Give the extent of all Plasmodium falciparum-infected red blood cells.
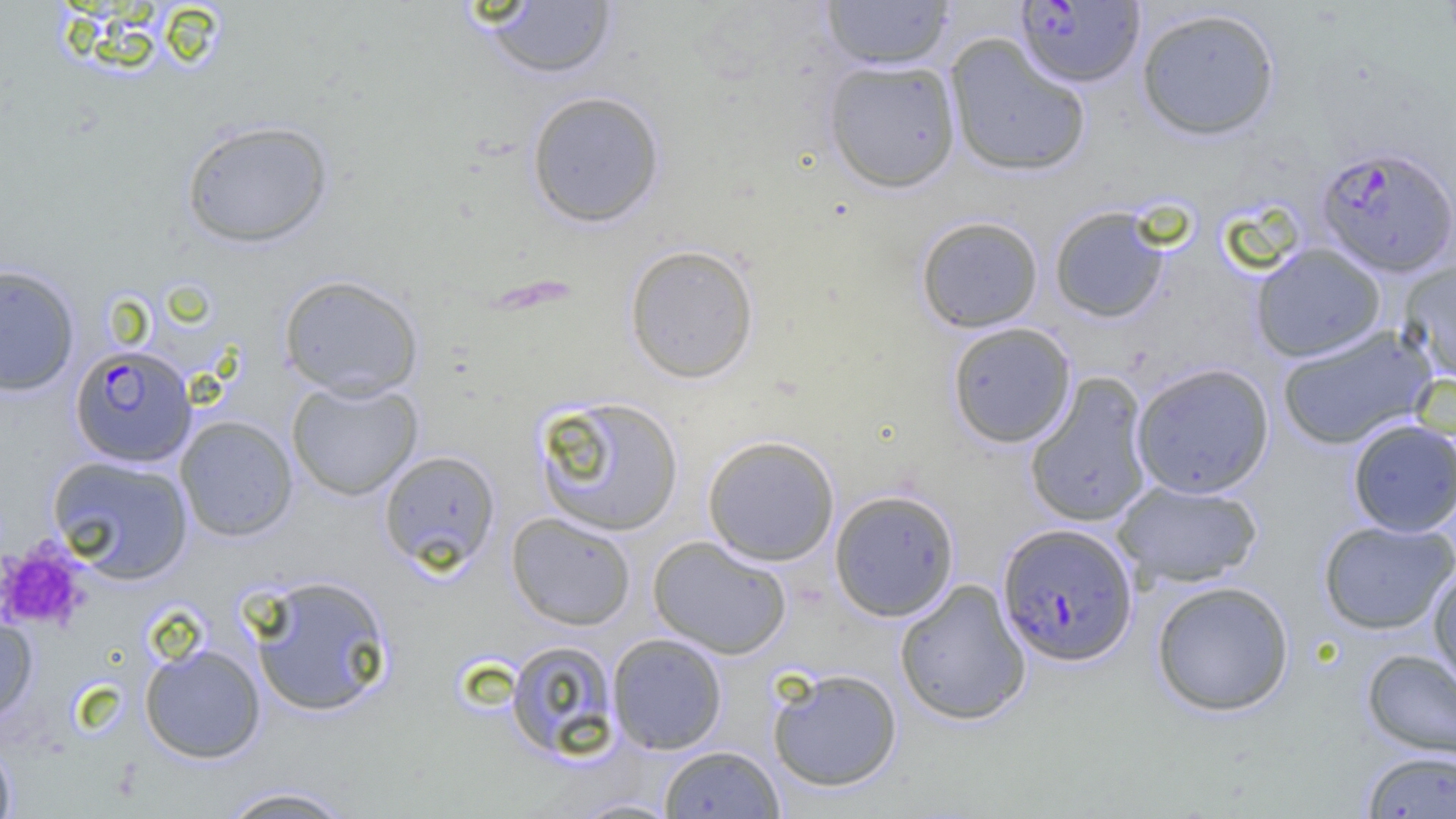

Approximate bounding boxes as [x1, y1, x2, y2] in pixels.
Plasmodium falciparum-infected red blood cells: [1016, 1, 1145, 88], [1316, 145, 1455, 278], [70, 344, 197, 467], [997, 523, 1138, 667].

slide-level diagnosis = Plasmodium falciparum
magnification = 1000x
field of view = single
modality = light microscopy
image size = 1456×819 pixels
uninfected red blood cell locations = approximate bounding boxes as [x1, y1, x2, y2] in pixels: [821, 0, 953, 70], [482, 1, 618, 80], [1136, 7, 1281, 141], [945, 33, 1091, 178], [823, 59, 961, 193], [526, 90, 666, 228], [180, 119, 333, 249], [1049, 206, 1170, 323], [915, 215, 1044, 333], [624, 243, 760, 384], [1251, 243, 1387, 362], [1398, 259, 1456, 381], [0, 264, 80, 397], [279, 274, 424, 400], [946, 322, 1077, 448], [1276, 323, 1437, 451], [1131, 363, 1274, 499], [1024, 372, 1154, 529], [286, 379, 423, 500], [531, 395, 685, 537], [175, 415, 298, 542], [1347, 418, 1456, 537], [702, 434, 840, 567], [379, 450, 501, 572], [46, 455, 194, 584], [1112, 480, 1262, 588], [829, 488, 960, 621], [506, 512, 637, 630], [1318, 519, 1455, 634], [648, 536, 792, 659], [1428, 564, 1456, 694], [248, 574, 394, 717], [894, 578, 1031, 726], [1151, 580, 1294, 716], [0, 602, 39, 727], [606, 633, 728, 754], [504, 639, 621, 761], [139, 643, 266, 763], [1361, 648, 1456, 762], [766, 667, 902, 792], [0, 738, 17, 819], [658, 745, 785, 818], [1360, 750, 1456, 818], [215, 785, 359, 818], [570, 796, 683, 818]
platelet locations = approximate bounding boxes as [x1, y1, x2, y2] in pixels: [0, 540, 90, 634]
preparation = thin blood smear